Report the malaria status of this cell.
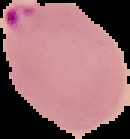
Parasitized.

{
  "image_size": "130×139 pixels",
  "image_type": "segmented cell region with the area outside set to black",
  "preparation": "thin blood smear"
}